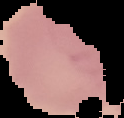
{
  "result": "no malaria parasites detected",
  "preparation": "thin blood smear",
  "image_type": "cell region segmented out of the field of view; surrounding area masked to black",
  "image_size": "124×118 pixels"
}